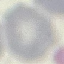
Summary:
  - Result: no malaria parasites seen
  - Preparation: thin blood film
  - Image type: automatically extracted cell patch, resized to 64 × 64 pixels
  - Capture: smartphone camera at the microscope eyepiece
  - Stain: Giemsa